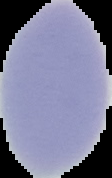
Segmented cell region on a black background. Image is 112×178 pixels. Result: negative for Plasmodium parasites. From a thin blood film.